State which cell type is depicted.
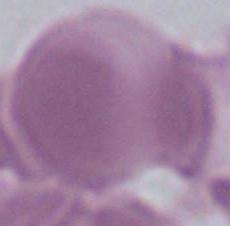

An erythrocyte.

magnification = 1000x
modality = micrograph